Mark where platelets are.
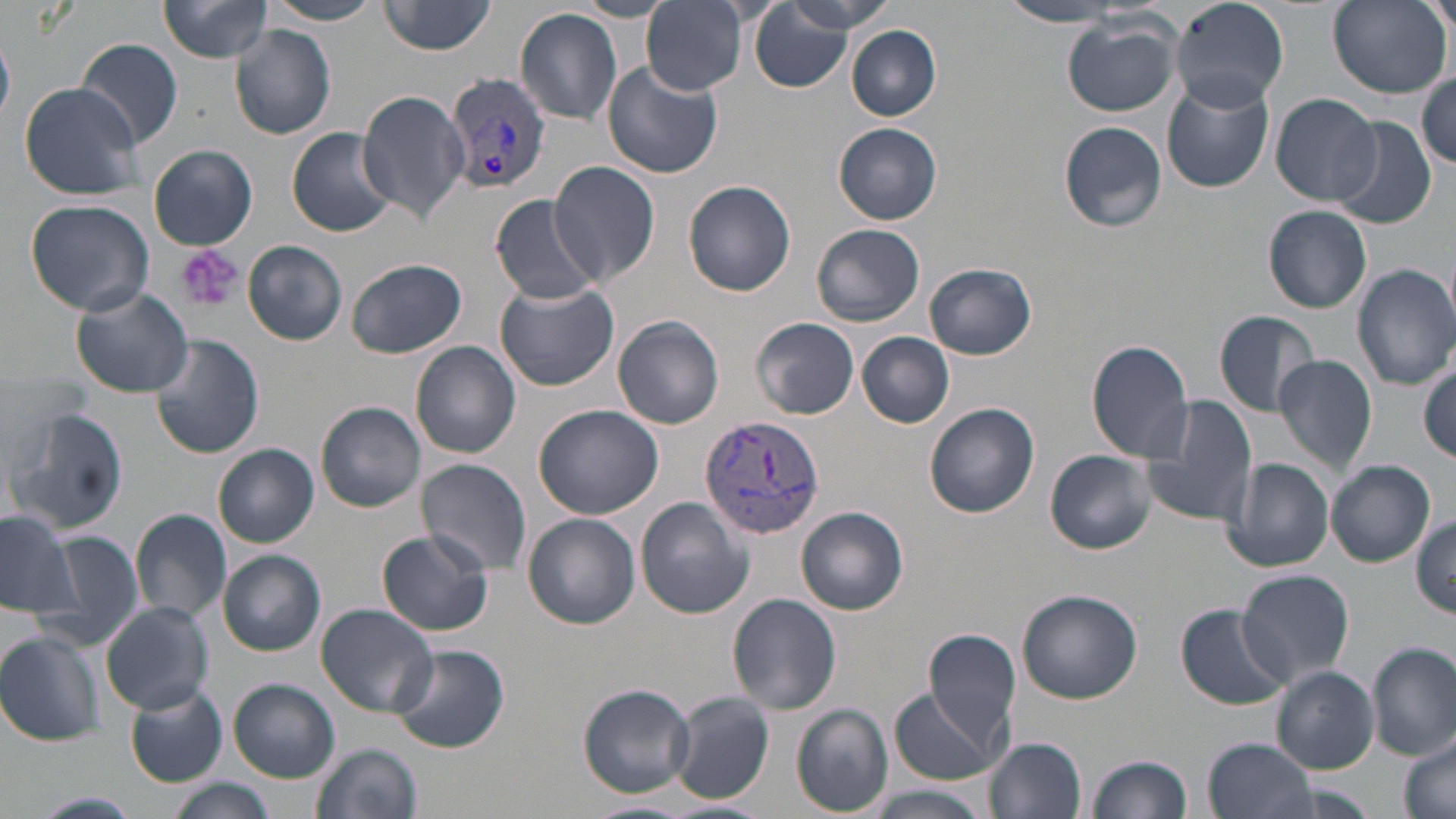
Approximate bounding boxes as (x1,y1)-(x2,y2) corner pairs in pixels.
Platelets: (176,244)-(243,312).

Plasmodium vivax-infected red blood cell locations: (443,70)-(552,197), (698,415)-(823,542). Uninfected red blood cell locations: (157,0)-(277,64), (261,0)-(386,25), (639,0)-(750,95), (775,0)-(896,36), (1169,0)-(1287,111), (1420,0)-(1456,39), (378,1)-(498,56), (569,1)-(676,22), (1328,1)-(1451,99), (998,3)-(1132,28), (748,5)-(857,89), (516,8)-(623,125), (1061,15)-(1182,117), (230,25)-(336,140), (847,26)-(942,121), (76,38)-(183,148), (603,60)-(725,180), (1415,72)-(1455,169), (1161,78)-(1274,193), (18,81)-(146,201), (357,88)-(470,223), (1271,93)-(1382,205), (1331,117)-(1437,229), (1058,120)-(1168,233), (834,123)-(942,224), (287,127)-(400,237), (149,145)-(257,250), (549,160)-(661,288), (683,179)-(796,296), (492,195)-(600,305), (25,198)-(155,316), (1262,206)-(1372,314), (813,223)-(925,327), (243,240)-(348,345), (346,258)-(467,358), (925,262)-(1037,359), (1353,262)-(1456,391), (494,280)-(619,390), (71,286)-(193,399), (1212,309)-(1319,418), (612,315)-(725,430), (751,317)-(859,419), (150,333)-(263,460), (857,333)-(955,429), (1086,339)-(1195,463), (411,342)-(521,458), (1274,355)-(1378,477), (1415,366)-(1456,464), (1138,394)-(1259,528), (925,401)-(1040,518), (316,402)-(426,512), (534,404)-(662,519), (6,405)-(130,539), (214,444)-(319,547), (1047,449)-(1157,555), (1222,456)-(1335,573), (417,458)-(531,575), (1327,461)-(1435,567), (634,497)-(755,619), (795,505)-(908,616), (130,508)-(233,627), (0,512)-(81,617), (523,512)-(641,628), (1411,515)-(1455,618), (37,530)-(143,652), (376,530)-(494,637), (218,549)-(325,657), (1235,569)-(1355,688), (1017,589)-(1144,703), (728,594)-(843,714), (101,602)-(214,715), (315,603)-(438,717), (1176,605)-(1292,709), (924,630)-(1023,753), (0,632)-(105,746), (1368,642)-(1456,761), (390,645)-(510,754), (1272,667)-(1379,773), (229,679)-(340,782), (124,682)-(228,787), (579,684)-(695,797), (887,686)-(1007,784), (668,692)-(773,804), (791,704)-(894,817), (1399,732)-(1456,819), (986,736)-(1087,818), (1202,736)-(1319,819), (311,742)-(423,819), (1085,753)-(1193,819), (162,779)-(279,819), (868,785)-(987,819), (25,792)-(143,818), (582,800)-(698,819). Slide-level diagnosis: Plasmodium vivax. Image is 1456×819 pixels. One field of a larger specimen. 1000x magnification. May-Grünwald-Giemsa-stained preparation. Thin blood film. Light microscopy.